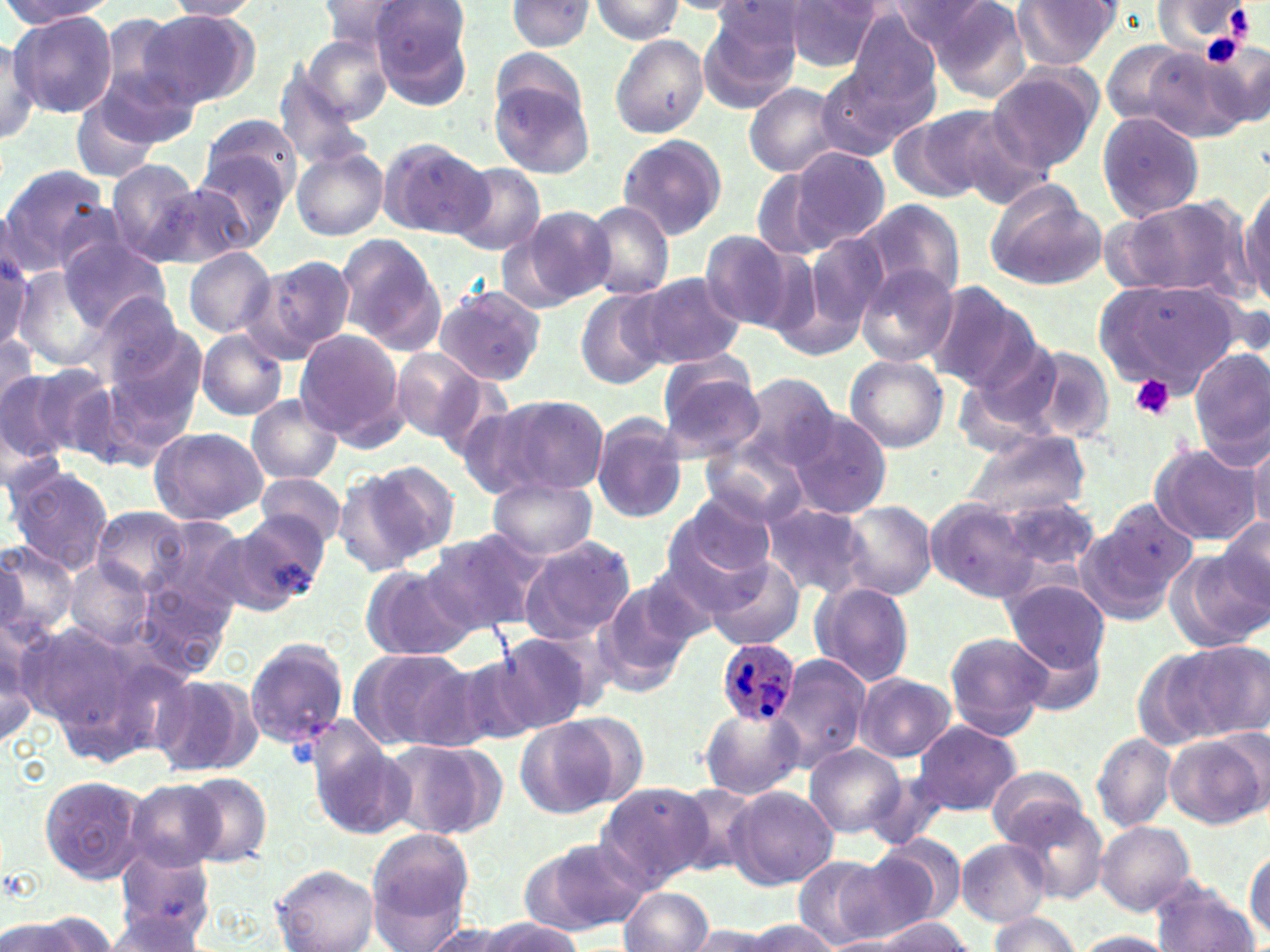

{
  "slide_level_diagnosis": "Plasmodium ovale",
  "platelet_locations": "approximate bounding boxes as [x1, y1, x2, y2] in pixels: [1225, 5, 1255, 42], [1200, 33, 1244, 68], [1130, 375, 1174, 418]",
  "preparation": "thin blood film",
  "stain": "May-Grünwald-Giemsa",
  "field_of_view": "one of a larger specimen",
  "modality": "light microscopy",
  "magnification": "1000x",
  "plasmodium_ovale_infected_red_blood_cell_locations": "approximate bounding boxes as [x1, y1, x2, y2] in pixels: [716, 637, 801, 728]",
  "uninfected_red_blood_cell_locations": "approximate bounding boxes as [x1, y1, x2, y2] in pixels: [1, 0, 109, 32], [164, 0, 266, 19], [316, 0, 418, 49], [369, 0, 473, 99], [1011, 0, 1119, 69], [504, 1, 597, 52], [590, 1, 686, 43], [783, 1, 883, 71], [886, 1, 1000, 49], [702, 3, 802, 102], [926, 3, 1032, 102], [846, 8, 945, 110], [13, 12, 118, 118], [142, 12, 261, 108], [94, 20, 201, 132], [0, 34, 43, 145], [298, 34, 394, 125], [610, 34, 708, 138], [1104, 39, 1197, 126], [1201, 39, 1270, 130], [1144, 48, 1252, 140], [818, 65, 926, 160], [986, 65, 1102, 173], [276, 69, 374, 170], [490, 78, 596, 181], [742, 81, 848, 177], [73, 94, 162, 184], [904, 104, 1018, 202], [947, 110, 1055, 210], [1096, 111, 1206, 223], [200, 113, 302, 202], [617, 134, 728, 239], [376, 137, 491, 239], [292, 145, 389, 241], [195, 148, 293, 251], [789, 148, 890, 249], [106, 159, 203, 263], [448, 163, 546, 255], [0, 164, 110, 275], [751, 169, 833, 262], [1237, 175, 1270, 307], [154, 178, 261, 269], [983, 182, 1106, 291], [1105, 194, 1250, 300], [857, 201, 962, 300], [580, 202, 675, 300], [515, 205, 615, 306], [698, 230, 800, 330], [333, 233, 446, 354], [800, 233, 890, 336], [59, 241, 170, 330], [183, 247, 277, 338], [249, 254, 354, 362], [2, 256, 36, 353], [857, 265, 958, 368], [12, 270, 107, 369], [632, 273, 745, 370], [1092, 278, 1242, 395], [923, 283, 1035, 391], [432, 286, 548, 385], [574, 289, 668, 389], [88, 290, 189, 390], [0, 330, 41, 409], [196, 330, 288, 421], [294, 331, 408, 445], [103, 342, 205, 460], [1020, 343, 1117, 443], [1188, 346, 1270, 462], [959, 347, 1065, 452], [390, 349, 487, 442], [844, 354, 950, 453], [26, 362, 119, 459], [658, 363, 766, 460], [0, 371, 71, 463], [732, 373, 840, 473], [245, 394, 341, 485], [487, 394, 610, 495], [590, 411, 690, 525], [786, 411, 894, 520], [149, 427, 267, 525], [962, 432, 1090, 518], [1245, 436, 1270, 536], [701, 443, 810, 530], [1149, 443, 1262, 548], [343, 459, 462, 568], [4, 464, 115, 574], [255, 471, 348, 548], [489, 476, 597, 559], [991, 492, 1101, 571], [668, 493, 778, 585], [926, 498, 1038, 602], [759, 501, 871, 600], [835, 501, 937, 599], [1079, 501, 1195, 622], [91, 506, 193, 593], [229, 510, 328, 608], [1214, 514, 1270, 611], [153, 517, 247, 610], [424, 528, 551, 635], [652, 532, 774, 627], [517, 536, 636, 645], [0, 540, 76, 641], [1167, 551, 1268, 650], [708, 556, 804, 650], [64, 560, 155, 648], [361, 565, 476, 662], [595, 577, 702, 696], [1002, 578, 1110, 675], [810, 582, 915, 688], [134, 584, 237, 677], [0, 615, 55, 739], [15, 625, 135, 733], [944, 631, 1051, 738], [243, 636, 349, 749], [492, 637, 589, 736], [1175, 640, 1266, 738], [347, 645, 474, 751], [772, 653, 870, 774], [452, 657, 545, 750], [153, 673, 258, 774], [855, 673, 956, 762], [698, 706, 803, 798], [515, 718, 616, 819], [911, 721, 1022, 815], [309, 728, 412, 841], [1165, 732, 1267, 829], [1091, 733, 1177, 831], [383, 741, 487, 838], [804, 743, 906, 839], [985, 767, 1090, 846], [181, 772, 273, 868], [39, 775, 148, 883], [123, 781, 224, 872], [666, 782, 765, 878], [595, 783, 710, 891], [724, 785, 838, 890], [1006, 801, 1109, 905], [1096, 821, 1195, 914], [367, 828, 475, 940], [865, 834, 966, 929], [523, 837, 651, 935], [955, 838, 1052, 926], [1246, 846, 1270, 942], [830, 851, 940, 943], [109, 856, 219, 948], [790, 856, 893, 948], [273, 864, 379, 952], [1153, 879, 1258, 952], [619, 887, 713, 952], [23, 911, 121, 952], [101, 911, 210, 952], [986, 913, 1082, 951], [864, 915, 974, 949], [475, 918, 586, 951], [1, 919, 79, 950], [743, 919, 836, 952], [418, 920, 520, 952], [683, 923, 778, 952], [1070, 931, 1176, 952]",
  "image_size": "1270×952 pixels"
}